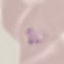
Summary:
  - Result: malaria parasites identified
  - Image type: cell patch, automatically extracted from a larger field of view and resized to 64 × 64 pixels
  - Stain: Giemsa
  - Preparation: thin blood film
  - Capture: smartphone camera at the microscope eyepiece